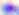
400x magnification. Toxoplasma gondii is seen. Photomicrograph.